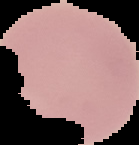
image type = cell region segmented out of the field of view; surrounding area masked to black
image size = 139×145 pixels
result = no Plasmodium parasites detected
preparation = thin blood film